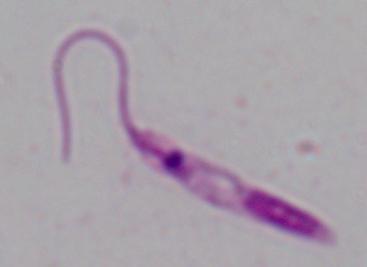

{
  "magnification": "1000x",
  "identification": "Leishmania",
  "modality": "photomicrograph"
}